Assess the morphology of the red blood cells.
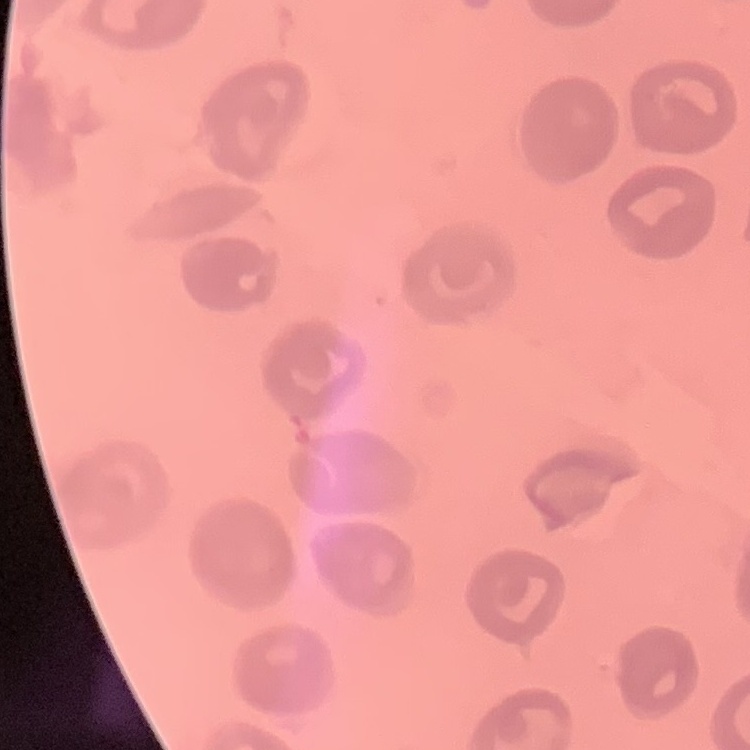

No rouleaux formation.

{
  "preparation": "thin blood film",
  "image_type": "one tile cut from a larger photomicrograph",
  "stain": "Field's or Giemsa"
}